Name the blood parasite species.
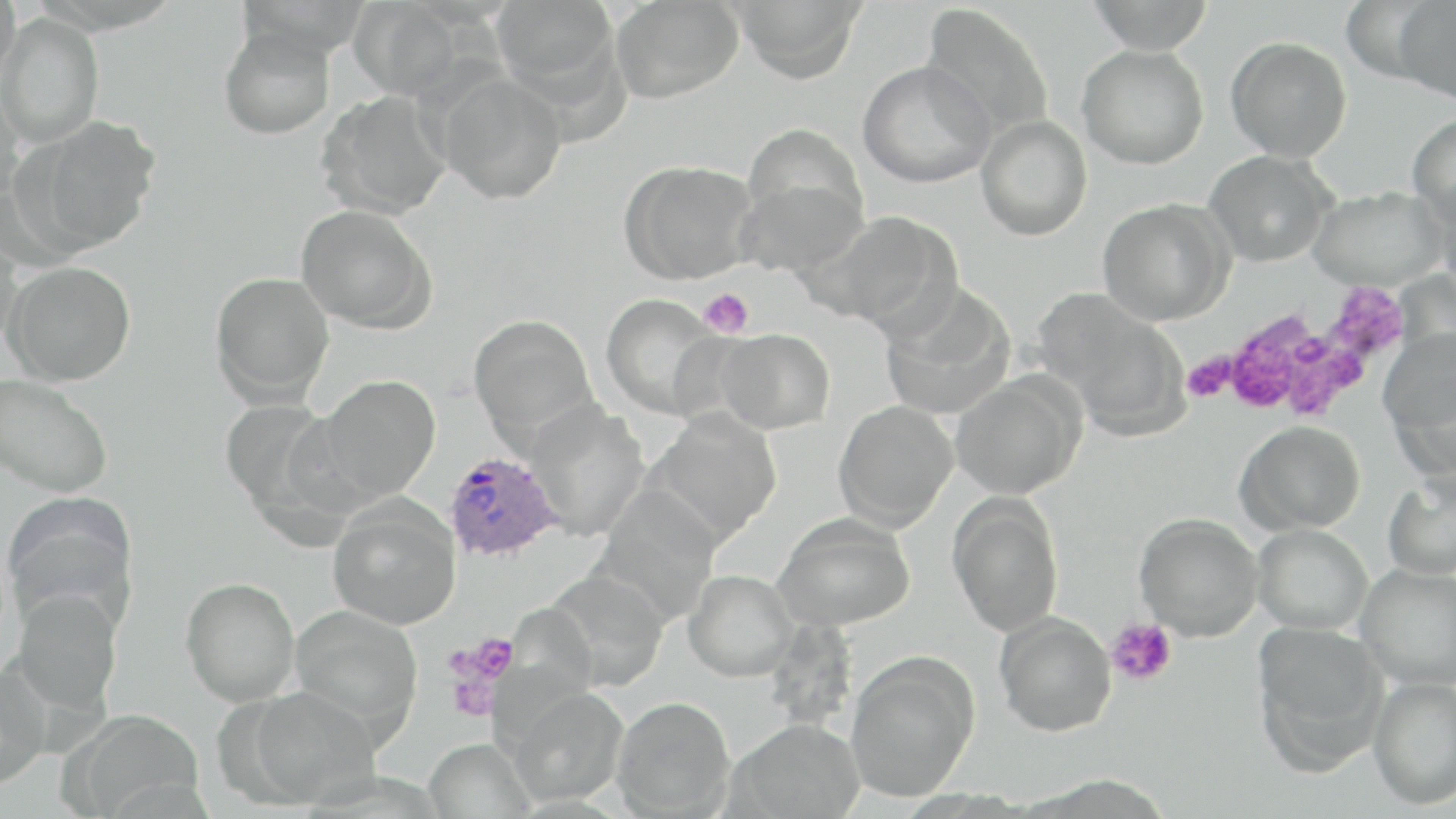
Plasmodium ovale.

Summary:
  - Coordinate format: approximate bounding boxes as [x1, y1, x2, y2] in pixels
  - Platelet locations: [1201, 287, 1413, 426], [699, 288, 754, 338], [1107, 618, 1177, 686], [460, 634, 519, 686], [445, 656, 503, 721]
  - Uninfected red blood cell locations: [1, 0, 20, 85], [611, 0, 744, 103], [728, 0, 868, 84], [1085, 0, 1217, 54], [346, 1, 464, 101], [1392, 1, 1456, 105], [491, 2, 620, 100], [921, 3, 1055, 141], [0, 12, 105, 148], [218, 24, 337, 140], [1225, 36, 1352, 161], [1077, 44, 1209, 169], [858, 59, 996, 189], [435, 71, 568, 204], [0, 89, 25, 208], [317, 90, 452, 220], [1407, 113, 1456, 225], [22, 115, 162, 253], [975, 115, 1092, 241], [741, 121, 868, 241], [1204, 149, 1336, 267], [619, 159, 758, 284], [733, 172, 865, 278], [1308, 186, 1448, 291], [1439, 190, 1456, 309], [1097, 198, 1234, 326], [295, 204, 437, 334], [804, 211, 957, 333], [0, 228, 22, 354], [3, 261, 137, 387], [209, 271, 335, 406], [878, 287, 1017, 420], [600, 294, 726, 418], [1038, 295, 1188, 435], [468, 313, 598, 445], [715, 327, 835, 434], [1378, 327, 1456, 460], [0, 374, 113, 498], [315, 375, 441, 503], [949, 375, 1084, 499], [218, 398, 339, 518], [833, 400, 958, 531], [525, 403, 650, 541], [646, 410, 782, 543], [1235, 420, 1365, 534], [1382, 473, 1456, 582], [593, 487, 723, 621], [1, 492, 140, 634], [947, 493, 1065, 637], [327, 497, 462, 629], [773, 512, 915, 630], [1134, 512, 1263, 641], [1252, 523, 1372, 634], [1356, 563, 1456, 690], [684, 569, 798, 682], [541, 570, 669, 690], [181, 577, 301, 707], [9, 588, 124, 718], [289, 606, 423, 734], [994, 611, 1117, 736], [1251, 621, 1387, 767], [844, 653, 979, 801], [0, 663, 52, 790], [1368, 676, 1456, 810], [503, 684, 628, 806], [242, 685, 380, 807], [611, 696, 735, 817], [65, 708, 204, 817], [728, 718, 865, 819], [423, 738, 535, 819]
  - Plasmodium ovale-infected red blood cell locations: [443, 451, 562, 563]
  - Image size: 1456×819 pixels
  - Modality: light microscopy
  - Stain: May-Grünwald-Giemsa
  - Field of view: single
  - Preparation: thin blood film
  - Magnification: 1000x